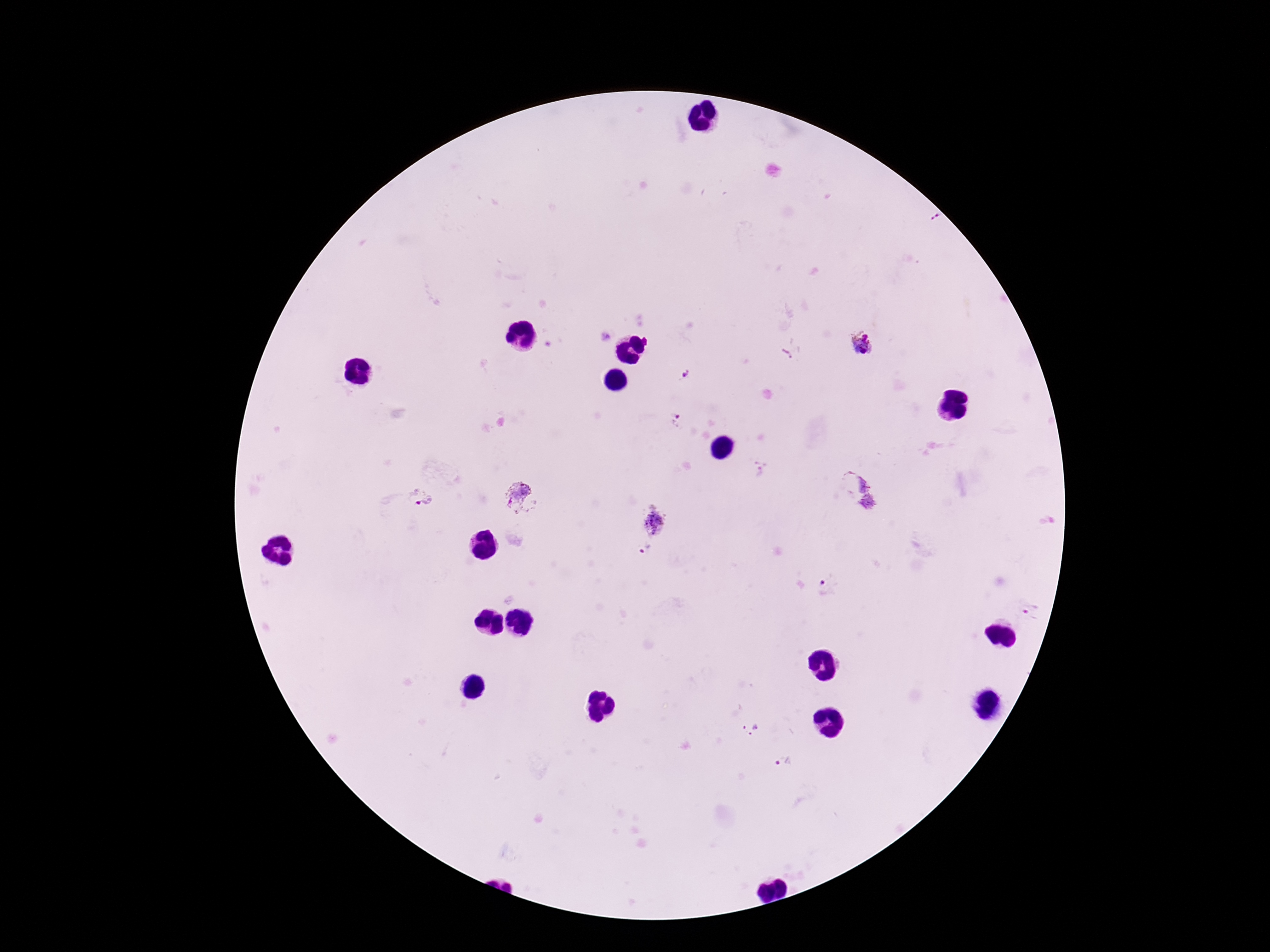
stain: Giemsa
field_of_view: single
patient_malaria_status: positive
capture: smartphone camera through the microscope eyepiece
magnification: 100x
preparation: thick peripheral-blood smear
plasmodium_parasite_locations: 'approximate centers as {x, y} in pixels: {862, 344}, {787, 353}, {686, 375}, {678, 421}, {760, 469}, {859, 490}, {518, 496}, {419, 499}, {654, 525}, {645, 548}, {827, 586}, {1033, 609}, {749, 728}, {784, 761}'
image_size: 1270×952 pixels